Locate every blood parasite and identify its species.
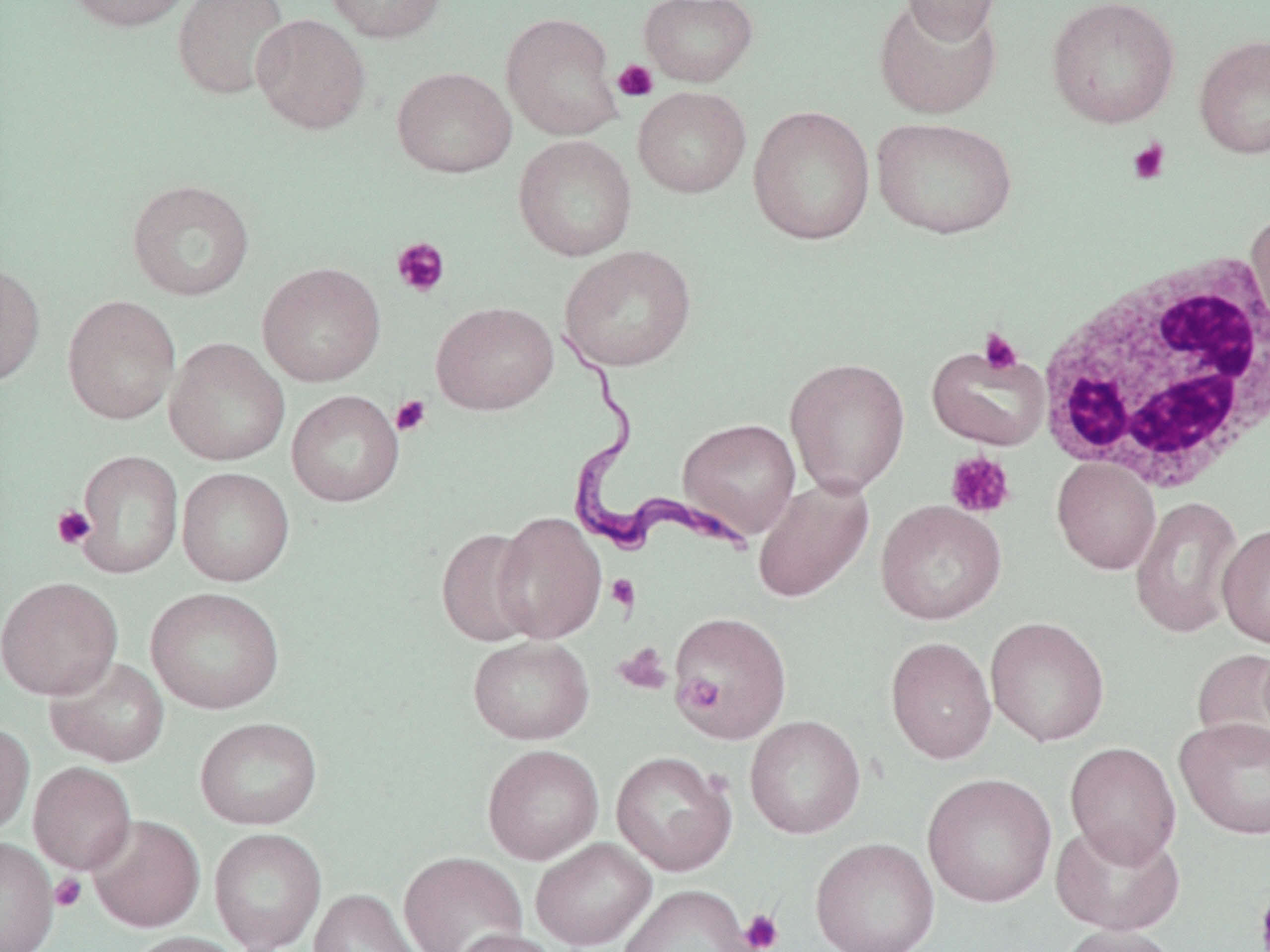

Approximate bounding boxes as [x1, y1, x2, y2] in pixels.
Trypanosoma brucei: [551, 332, 756, 563].
No Plasmodium falciparum, Plasmodium ovale, Plasmodium malariae, Plasmodium vivax, or Babesia divergens observed.

Platelet locations: [612, 59, 659, 102], [1127, 138, 1171, 185], [391, 237, 450, 298], [978, 328, 1024, 374], [390, 395, 432, 436], [945, 451, 1016, 519], [52, 505, 95, 549], [605, 574, 640, 613], [613, 642, 672, 695], [679, 676, 725, 713], [49, 873, 87, 912], [1255, 881, 1270, 952], [739, 909, 784, 952]. Uninfected red blood cell locations: [64, 0, 195, 32], [172, 0, 291, 101], [324, 0, 448, 43], [638, 0, 758, 87], [901, 0, 1002, 45], [1046, 0, 1181, 129], [873, 1, 1002, 120], [501, 12, 622, 140], [251, 13, 371, 135], [1193, 33, 1270, 160], [391, 66, 517, 178], [632, 86, 751, 198], [748, 105, 876, 245], [871, 116, 1017, 239], [513, 134, 637, 261], [126, 179, 255, 302], [1246, 208, 1270, 337], [559, 245, 697, 372], [0, 261, 46, 387], [257, 261, 386, 387], [62, 294, 181, 425], [431, 301, 558, 414], [164, 337, 289, 466], [926, 344, 1050, 450], [784, 357, 910, 497], [286, 390, 404, 507], [678, 418, 801, 539], [74, 449, 184, 578], [1052, 458, 1161, 574], [177, 467, 294, 586], [752, 477, 874, 603], [1129, 495, 1244, 639], [875, 499, 1007, 625], [493, 511, 607, 643], [1217, 523, 1270, 649], [436, 528, 540, 647], [0, 576, 122, 700], [145, 586, 285, 715], [669, 610, 792, 743], [985, 616, 1110, 747], [467, 636, 594, 744], [885, 636, 997, 765], [1191, 647, 1270, 761], [45, 655, 170, 767], [744, 715, 865, 839], [194, 716, 323, 830], [1174, 716, 1270, 840], [0, 722, 34, 836], [1065, 742, 1181, 867], [482, 743, 603, 864], [610, 750, 737, 876], [29, 761, 136, 875], [922, 772, 1057, 908], [86, 814, 205, 933], [1050, 820, 1186, 936], [209, 828, 326, 952], [0, 836, 59, 952], [810, 836, 940, 952], [530, 838, 656, 951], [398, 850, 528, 952], [617, 885, 754, 952], [309, 888, 422, 952], [1058, 924, 1181, 952], [450, 928, 564, 952], [123, 931, 248, 952]. White blood cell locations: [1033, 250, 1270, 494]. Slide-level diagnosis: Trypanosoma brucei. May-Grünwald-Giemsa-stained preparation. Optical microscopy. Captured at 1000x magnification. Image is 1270×952 pixels. Thin blood film. One field of a larger specimen.